Point out each leukocyte.
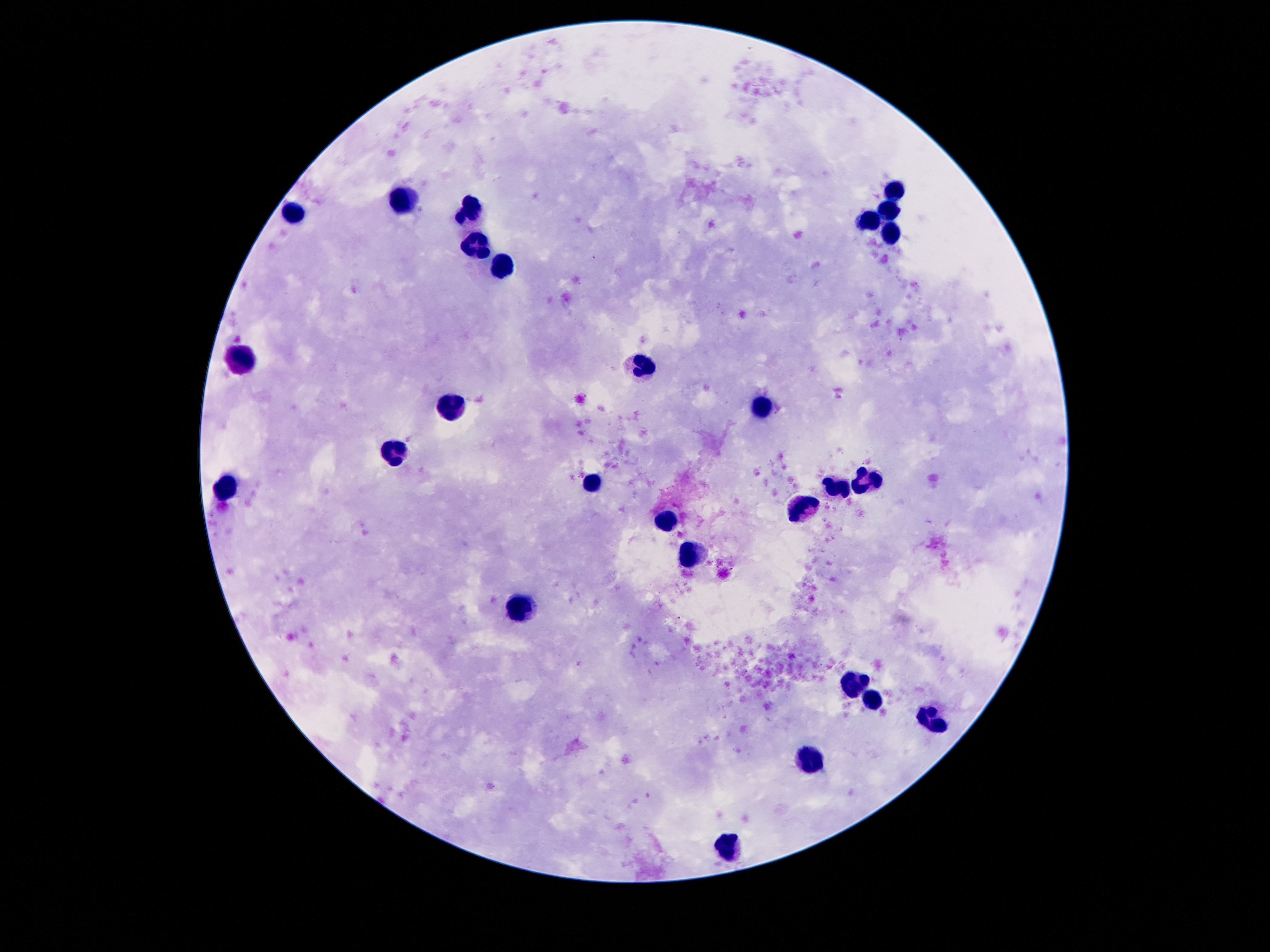
Approximate centers as [x, y] in pixels.
Leukocytes: [899, 190], [409, 200], [469, 209], [889, 209], [292, 211], [869, 220], [889, 231], [480, 248], [503, 261], [245, 362], [639, 368], [764, 402], [449, 407], [398, 452], [869, 480], [594, 481], [837, 486], [225, 489], [803, 509], [667, 521], [691, 554], [523, 606], [854, 686], [872, 701], [928, 718], [811, 759], [732, 843].

Summary:
  - Capture: smartphone camera through the microscope eyepiece
  - Patient malaria status: uninfected
  - Magnification: 100x
  - Field of view: one from this slide
  - Stain: Giemsa
  - Image size: 1270×952 pixels
  - Preparation: thick peripheral-blood smear